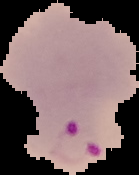

Summary:
  - Malaria status: parasitized
  - Image type: segmented cell region with the area outside set to black
  - Preparation: thin blood smear
  - Image size: 139×175 pixels